Identify the blood parasite species.
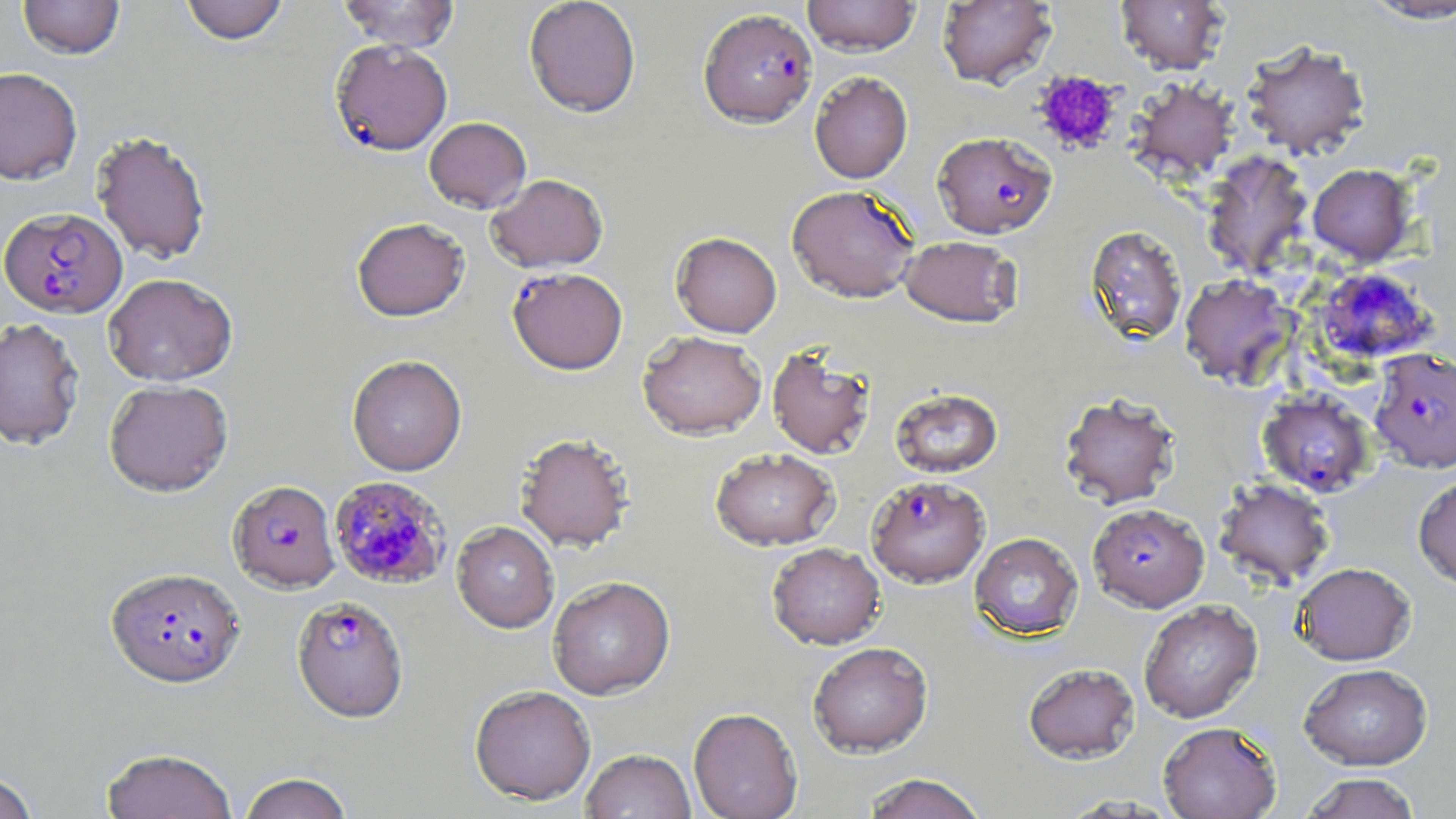
Plasmodium falciparum.

Summary:
  - Coordinate format: approximate bounding boxes as (x1,y1)-(x2,y2) corner pairs in pixels
  - Plasmodium falciparum-infected red blood cell locations: (698,8)-(817,128), (330,39)-(453,156), (932,131)-(1057,238), (0,203)-(127,315), (507,266)-(628,375), (1313,267)-(1438,365), (1369,348)-(1455,473), (1257,388)-(1375,497), (866,475)-(990,588), (329,476)-(453,591), (227,479)-(340,593), (1088,502)-(1209,612), (106,567)-(246,690), (292,595)-(408,722)
  - Platelet locations: (1032,70)-(1122,156)
  - Uninfected red blood cell locations: (17,0)-(125,59), (179,0)-(289,45), (337,0)-(459,51), (524,0)-(641,117), (802,0)-(921,56), (936,0)-(1057,89), (1116,0)-(1229,75), (1359,1)-(1456,24), (1241,40)-(1371,160), (0,67)-(83,185), (809,71)-(913,184), (1126,77)-(1240,184), (424,117)-(531,213), (91,130)-(212,264), (1201,150)-(1313,279), (1307,163)-(1416,265), (485,173)-(609,273), (787,184)-(920,303), (352,217)-(470,322), (1084,224)-(1188,346), (670,232)-(782,337), (900,235)-(1023,328), (103,273)-(237,386), (1179,273)-(1296,388), (0,317)-(85,451), (637,330)-(767,440), (767,344)-(876,459), (347,354)-(467,476), (104,379)-(233,496), (890,387)-(1003,478), (1058,391)-(1182,509), (515,432)-(634,552), (710,448)-(839,551), (1413,474)-(1456,591), (1214,477)-(1335,588), (452,520)-(559,633), (970,532)-(1083,641), (767,542)-(885,649), (1292,561)-(1416,665), (547,575)-(675,700), (1138,599)-(1262,723), (807,641)-(933,757), (1023,662)-(1139,764), (1299,663)-(1432,770), (469,684)-(596,805), (688,707)-(803,819), (1158,720)-(1282,819), (101,748)-(237,819), (580,748)-(696,819), (0,771)-(39,819), (239,772)-(354,819), (862,772)-(988,819), (1301,772)-(1422,818), (1056,794)-(1183,817)
  - Magnification: 1000x
  - Image size: 1456×819 pixels
  - Stain: May-Grünwald-Giemsa
  - Preparation: thin blood film
  - Field of view: one of a larger specimen
  - Modality: optical microscopy